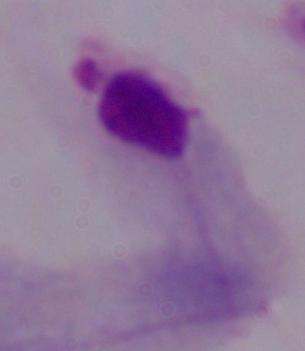
Summary:
  - Magnification: 1000x
  - Modality: photomicrograph
  - Identification: trichomonad